Comment on the morphology of the erythrocytes.
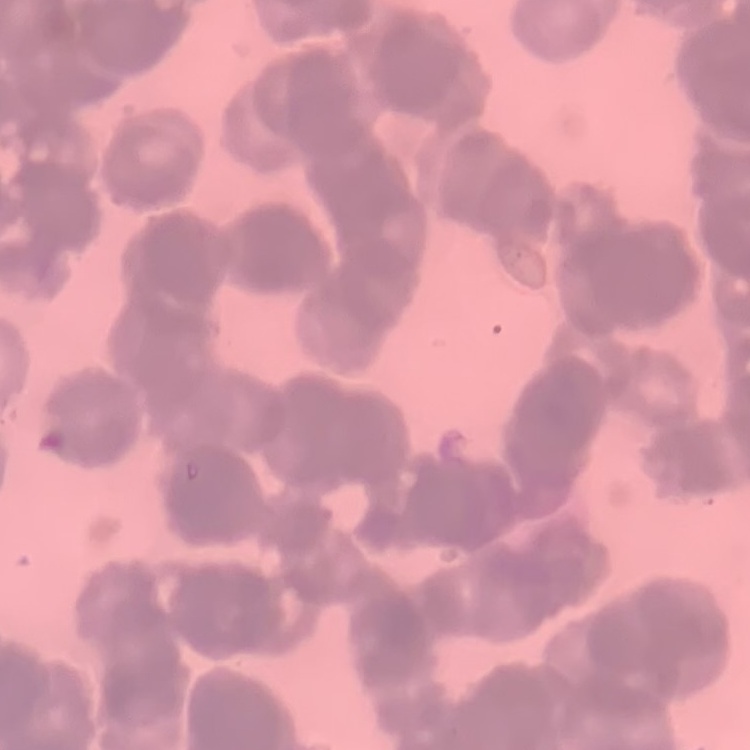
They show rouleaux formation.

Stained with either Field's or Giemsa. Square crop of a larger photomicrograph. Thin blood smear.